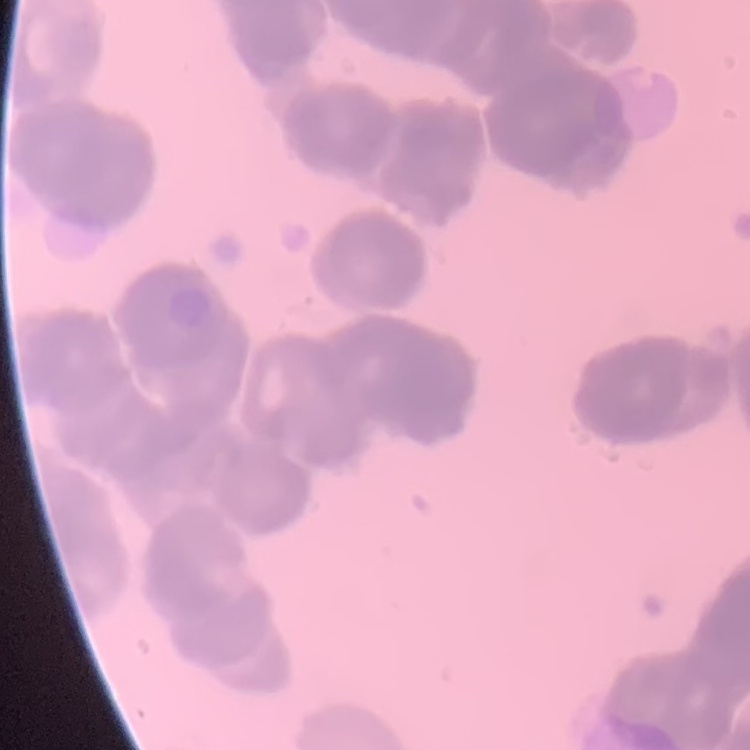

red blood cell morphology = rouleaux formation
preparation = thin blood film
image type = square crop of a larger photomicrograph
stain = Field's or Giemsa